Classify this cell by malaria status.
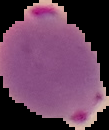
It is parasitized.

Image is 109×130 pixels. Cell region segmented out of the field of view; the surrounding area is masked to black. From a thin blood film.